Identify the cell.
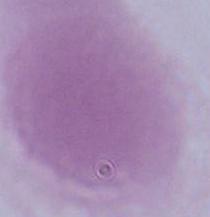

An erythrocyte.

magnification: 1000x
modality: micrograph